Classify this cell by malaria status.
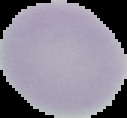
Uninfected.

The area outside the segmented cell region is set to black. From a thin blood film. Image is 127×118 pixels.